Assess this cell for malaria.
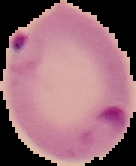
It is parasitized.

Cell region segmented out of the field of view; the surrounding area is masked to black. From a thin blood film. Image is 136×166 pixels.